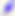
Summary:
  - Modality: photomicrograph
  - Magnification: 400x
  - Identification: Toxoplasma gondii